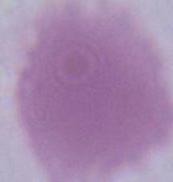 A red blood cell is seen. Micrograph. Captured at 1000x magnification.